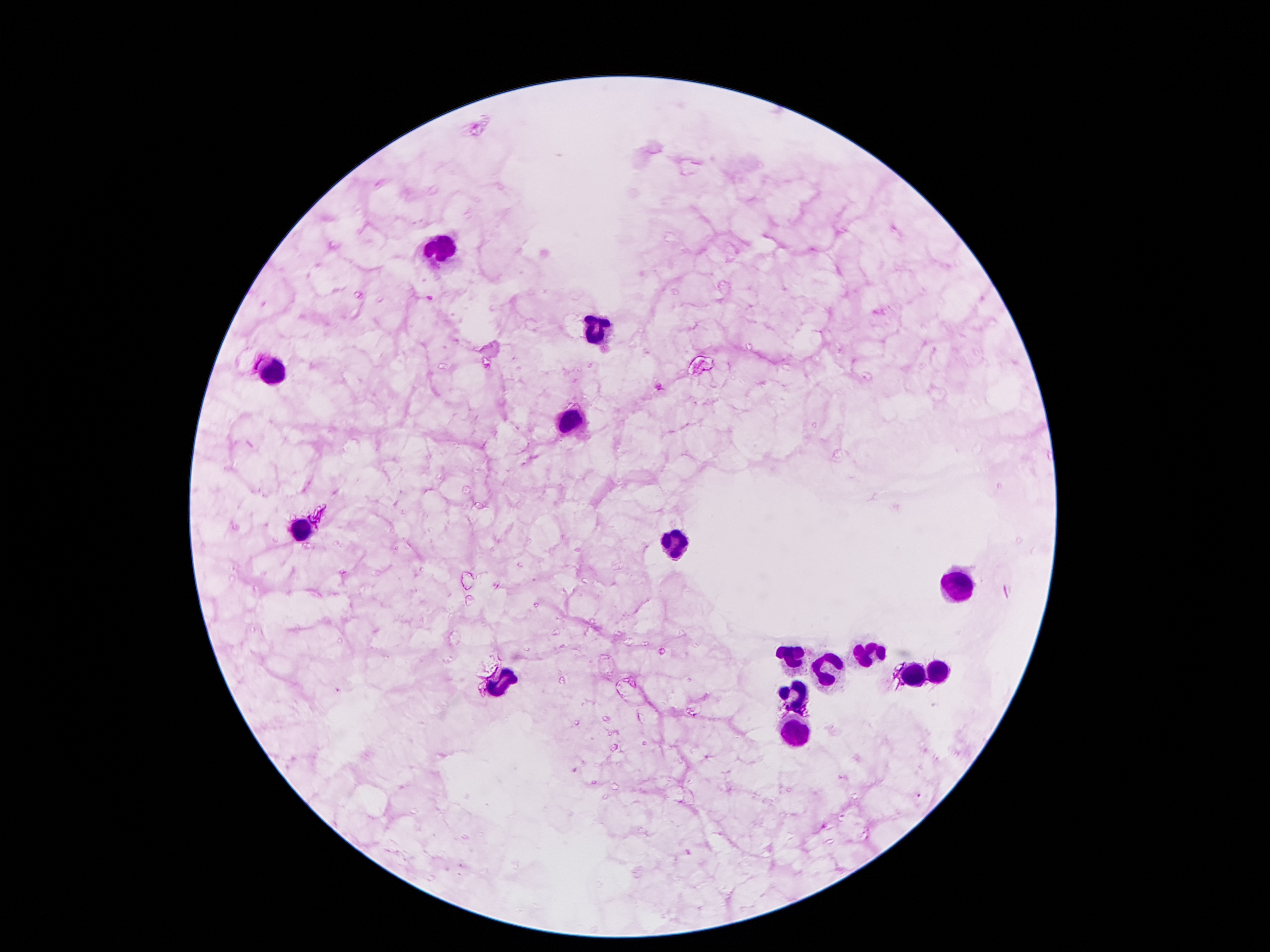

Approximate centers as [x, y] in pixels.
Summary:
  - Plasmodium parasite locations: [659, 387]
  - Leukocyte locations: [442, 247], [594, 331], [269, 372], [569, 419], [301, 533], [674, 546], [958, 589], [867, 655], [794, 657], [826, 673], [910, 673], [937, 676], [501, 682], [796, 696], [796, 728]
  - Capture: smartphone camera through the microscope eyepiece
  - Field of view: one from this slide
  - Image size: 1270×952 pixels
  - Preparation: thick blood smear
  - Magnification: 100x
  - Patient malaria status: infected with Plasmodium falciparum
  - Stain: Giemsa